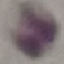

Result: no malaria parasites detected. Acquired by smartphone through the microscope eyepiece. Giemsa-stained preparation. Automatically extracted cell patch, resized to 64 × 64 pixels. Thin blood smear.